Assess this cell for malaria.
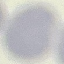

It is uninfected.

stain = Giemsa
capture = smartphone through the microscope eyepiece
image type = automatically extracted cell patch, resized to 64 × 64 pixels
preparation = thin blood smear